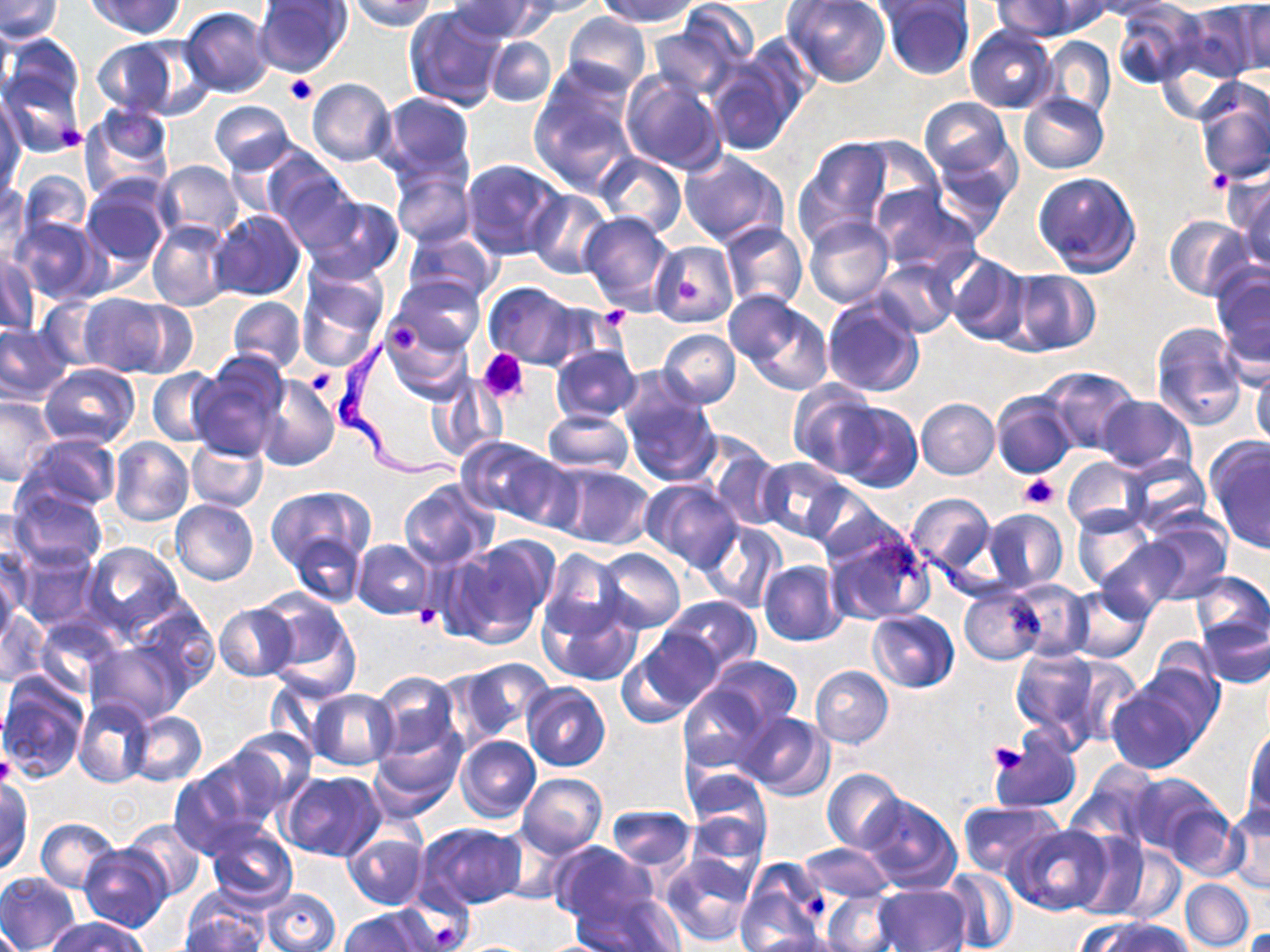
Summary:
  - Coordinate format: approximate bounding boxes as named x1/y1/x2/y2 corners in pixels
  - Trypanosoma brucei locations: (x1=329, y1=340, x2=460, y2=482)
  - Platelet locations: (x1=283, y1=75, x2=316, y2=104), (x1=61, y1=124, x2=88, y2=150), (x1=1207, y1=169, x2=1233, y2=193), (x1=678, y1=279, x2=699, y2=300), (x1=597, y1=310, x2=631, y2=332), (x1=383, y1=317, x2=425, y2=355), (x1=479, y1=349, x2=529, y2=403), (x1=306, y1=370, x2=336, y2=395), (x1=1020, y1=474, x2=1058, y2=509), (x1=412, y1=606, x2=440, y2=629), (x1=988, y1=742, x2=1025, y2=773), (x1=0, y1=754, x2=16, y2=788), (x1=804, y1=892, x2=831, y2=919), (x1=433, y1=922, x2=460, y2=946)
  - Uninfected red blood cell locations: (x1=0, y1=0, x2=63, y2=42), (x1=88, y1=0, x2=185, y2=38), (x1=346, y1=0, x2=438, y2=31), (x1=447, y1=0, x2=545, y2=42), (x1=513, y1=0, x2=606, y2=17), (x1=596, y1=0, x2=700, y2=28), (x1=782, y1=0, x2=891, y2=87), (x1=993, y1=0, x2=1088, y2=41), (x1=1082, y1=0, x2=1180, y2=20), (x1=253, y1=1, x2=355, y2=78), (x1=880, y1=1, x2=975, y2=81), (x1=1113, y1=1, x2=1205, y2=88), (x1=864, y1=2, x2=967, y2=24), (x1=1175, y1=2, x2=1266, y2=83), (x1=1231, y1=2, x2=1269, y2=77), (x1=403, y1=4, x2=508, y2=112), (x1=180, y1=7, x2=274, y2=97), (x1=647, y1=11, x2=753, y2=99), (x1=561, y1=12, x2=652, y2=94), (x1=965, y1=27, x2=1058, y2=113), (x1=95, y1=36, x2=200, y2=119), (x1=485, y1=36, x2=557, y2=107), (x1=1039, y1=37, x2=1116, y2=120), (x1=0, y1=56, x2=86, y2=159), (x1=704, y1=57, x2=801, y2=156), (x1=620, y1=69, x2=727, y2=175), (x1=307, y1=78, x2=395, y2=167), (x1=528, y1=79, x2=638, y2=192), (x1=1195, y1=81, x2=1270, y2=187), (x1=372, y1=92, x2=475, y2=183), (x1=1017, y1=92, x2=1110, y2=174), (x1=0, y1=97, x2=26, y2=194), (x1=920, y1=98, x2=1012, y2=179), (x1=210, y1=101, x2=295, y2=173), (x1=79, y1=108, x2=173, y2=203), (x1=797, y1=136, x2=893, y2=238), (x1=855, y1=138, x2=945, y2=217), (x1=929, y1=146, x2=1020, y2=236), (x1=680, y1=150, x2=790, y2=249), (x1=596, y1=153, x2=686, y2=238), (x1=263, y1=154, x2=357, y2=244), (x1=153, y1=159, x2=243, y2=244), (x1=460, y1=159, x2=568, y2=260), (x1=390, y1=166, x2=475, y2=249), (x1=0, y1=169, x2=28, y2=252), (x1=15, y1=169, x2=91, y2=246), (x1=1032, y1=170, x2=1142, y2=275), (x1=1227, y1=172, x2=1270, y2=268), (x1=81, y1=179, x2=171, y2=272), (x1=868, y1=186, x2=981, y2=274), (x1=526, y1=187, x2=614, y2=280), (x1=301, y1=194, x2=404, y2=282), (x1=211, y1=209, x2=306, y2=302), (x1=580, y1=212, x2=675, y2=313), (x1=11, y1=215, x2=107, y2=304), (x1=1165, y1=215, x2=1253, y2=300), (x1=804, y1=217, x2=894, y2=307), (x1=148, y1=219, x2=234, y2=312), (x1=719, y1=221, x2=808, y2=310), (x1=403, y1=230, x2=500, y2=307), (x1=649, y1=241, x2=738, y2=328), (x1=1, y1=248, x2=40, y2=338), (x1=946, y1=255, x2=1030, y2=345), (x1=872, y1=259, x2=960, y2=338), (x1=295, y1=266, x2=389, y2=370), (x1=1003, y1=269, x2=1100, y2=356), (x1=1212, y1=269, x2=1269, y2=373), (x1=390, y1=276, x2=487, y2=357), (x1=484, y1=282, x2=580, y2=367), (x1=723, y1=290, x2=804, y2=366), (x1=76, y1=293, x2=171, y2=375), (x1=36, y1=296, x2=111, y2=370), (x1=227, y1=296, x2=305, y2=372), (x1=736, y1=296, x2=833, y2=394), (x1=822, y1=298, x2=924, y2=398), (x1=112, y1=300, x2=198, y2=378), (x1=382, y1=320, x2=471, y2=403), (x1=0, y1=322, x2=70, y2=403), (x1=1150, y1=323, x2=1247, y2=430), (x1=658, y1=329, x2=739, y2=408), (x1=550, y1=346, x2=640, y2=423), (x1=190, y1=354, x2=288, y2=460), (x1=40, y1=362, x2=140, y2=448), (x1=1251, y1=363, x2=1270, y2=447), (x1=1041, y1=367, x2=1142, y2=454), (x1=146, y1=369, x2=223, y2=447), (x1=253, y1=375, x2=339, y2=471), (x1=428, y1=376, x2=508, y2=463), (x1=788, y1=380, x2=881, y2=475), (x1=621, y1=390, x2=721, y2=487), (x1=992, y1=391, x2=1077, y2=479), (x1=1095, y1=394, x2=1197, y2=478), (x1=0, y1=396, x2=59, y2=486), (x1=916, y1=398, x2=999, y2=479), (x1=833, y1=401, x2=922, y2=492), (x1=542, y1=408, x2=634, y2=475), (x1=19, y1=433, x2=122, y2=512), (x1=456, y1=437, x2=556, y2=519), (x1=110, y1=438, x2=195, y2=526), (x1=187, y1=438, x2=268, y2=512), (x1=1206, y1=438, x2=1270, y2=552), (x1=706, y1=444, x2=784, y2=530), (x1=1062, y1=456, x2=1149, y2=533), (x1=757, y1=457, x2=852, y2=543), (x1=1121, y1=457, x2=1210, y2=537), (x1=552, y1=464, x2=656, y2=550), (x1=397, y1=478, x2=499, y2=572), (x1=641, y1=479, x2=744, y2=573), (x1=266, y1=485, x2=374, y2=570), (x1=10, y1=489, x2=109, y2=569), (x1=806, y1=489, x2=903, y2=567), (x1=904, y1=493, x2=994, y2=575), (x1=171, y1=499, x2=258, y2=586), (x1=1071, y1=505, x2=1155, y2=593), (x1=0, y1=506, x2=41, y2=585), (x1=982, y1=508, x2=1068, y2=592), (x1=1140, y1=514, x2=1232, y2=602), (x1=699, y1=520, x2=785, y2=614), (x1=824, y1=530, x2=933, y2=626), (x1=289, y1=532, x2=366, y2=609), (x1=450, y1=535, x2=558, y2=646), (x1=1095, y1=537, x2=1186, y2=616), (x1=353, y1=539, x2=434, y2=619), (x1=82, y1=542, x2=184, y2=638), (x1=0, y1=544, x2=31, y2=630), (x1=11, y1=544, x2=100, y2=631), (x1=596, y1=548, x2=686, y2=633), (x1=540, y1=549, x2=628, y2=640), (x1=758, y1=560, x2=847, y2=646), (x1=0, y1=564, x2=20, y2=649), (x1=1189, y1=572, x2=1269, y2=647), (x1=1008, y1=581, x2=1091, y2=661), (x1=958, y1=586, x2=1046, y2=664), (x1=1069, y1=587, x2=1152, y2=662), (x1=261, y1=590, x2=358, y2=692), (x1=1052, y1=590, x2=1146, y2=725), (x1=661, y1=596, x2=760, y2=673), (x1=541, y1=597, x2=642, y2=686), (x1=124, y1=602, x2=219, y2=692), (x1=214, y1=602, x2=300, y2=682), (x1=2, y1=605, x2=50, y2=687), (x1=867, y1=609, x2=959, y2=693), (x1=33, y1=614, x2=126, y2=700), (x1=1196, y1=617, x2=1270, y2=689), (x1=618, y1=631, x2=723, y2=725), (x1=85, y1=640, x2=188, y2=726), (x1=1011, y1=646, x2=1100, y2=744), (x1=707, y1=656, x2=802, y2=737), (x1=453, y1=657, x2=554, y2=741), (x1=1065, y1=657, x2=1144, y2=747), (x1=1130, y1=660, x2=1224, y2=749), (x1=810, y1=666, x2=894, y2=748), (x1=370, y1=672, x2=461, y2=760), (x1=0, y1=674, x2=89, y2=783), (x1=1107, y1=679, x2=1208, y2=774), (x1=521, y1=683, x2=611, y2=772), (x1=677, y1=683, x2=774, y2=773), (x1=308, y1=689, x2=398, y2=770), (x1=73, y1=697, x2=154, y2=788), (x1=124, y1=711, x2=207, y2=786), (x1=734, y1=711, x2=835, y2=799), (x1=1243, y1=724, x2=1270, y2=823), (x1=232, y1=726, x2=318, y2=808), (x1=371, y1=727, x2=464, y2=817), (x1=989, y1=729, x2=1081, y2=814), (x1=455, y1=735, x2=541, y2=822), (x1=193, y1=745, x2=291, y2=831), (x1=167, y1=765, x2=271, y2=859), (x1=1066, y1=765, x2=1160, y2=847), (x1=683, y1=768, x2=773, y2=852), (x1=822, y1=768, x2=906, y2=853), (x1=280, y1=771, x2=385, y2=861), (x1=518, y1=772, x2=606, y2=856), (x1=1125, y1=772, x2=1225, y2=858), (x1=0, y1=778, x2=32, y2=875), (x1=858, y1=794, x2=960, y2=894), (x1=1160, y1=800, x2=1246, y2=880), (x1=956, y1=801, x2=1065, y2=878), (x1=1224, y1=804, x2=1270, y2=893), (x1=605, y1=806, x2=696, y2=872), (x1=683, y1=811, x2=769, y2=887), (x1=34, y1=818, x2=120, y2=892), (x1=121, y1=819, x2=206, y2=899), (x1=416, y1=823, x2=526, y2=910), (x1=1007, y1=824, x2=1111, y2=914), (x1=489, y1=825, x2=574, y2=903), (x1=206, y1=827, x2=297, y2=909), (x1=343, y1=828, x2=429, y2=910), (x1=1070, y1=830, x2=1154, y2=919), (x1=79, y1=843, x2=172, y2=932), (x1=549, y1=843, x2=654, y2=928), (x1=797, y1=843, x2=893, y2=904), (x1=1107, y1=844, x2=1187, y2=926), (x1=660, y1=853, x2=755, y2=948), (x1=734, y1=859, x2=828, y2=948), (x1=942, y1=869, x2=1020, y2=951), (x1=0, y1=871, x2=81, y2=952), (x1=1180, y1=879, x2=1254, y2=950), (x1=873, y1=883, x2=972, y2=952), (x1=261, y1=888, x2=340, y2=951), (x1=574, y1=891, x2=683, y2=952), (x1=821, y1=892, x2=905, y2=952), (x1=181, y1=900, x2=270, y2=951), (x1=338, y1=907, x2=441, y2=952), (x1=48, y1=916, x2=149, y2=952), (x1=1086, y1=917, x2=1191, y2=952), (x1=0, y1=920, x2=25, y2=952), (x1=748, y1=930, x2=849, y2=952)
  - Slide-level diagnosis: Trypanosoma brucei
  - Preparation: thin blood smear
  - Field of view: single
  - Modality: light microscopy
  - Magnification: 1000x
  - Image size: 1270×952 pixels
  - Stain: May-Grünwald-Giemsa